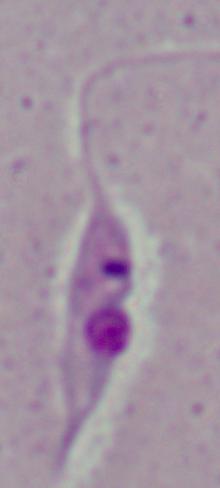

Summary:
  - Magnification: 1000x
  - Identification: Leishmania
  - Modality: photomicrograph